Locate cells.
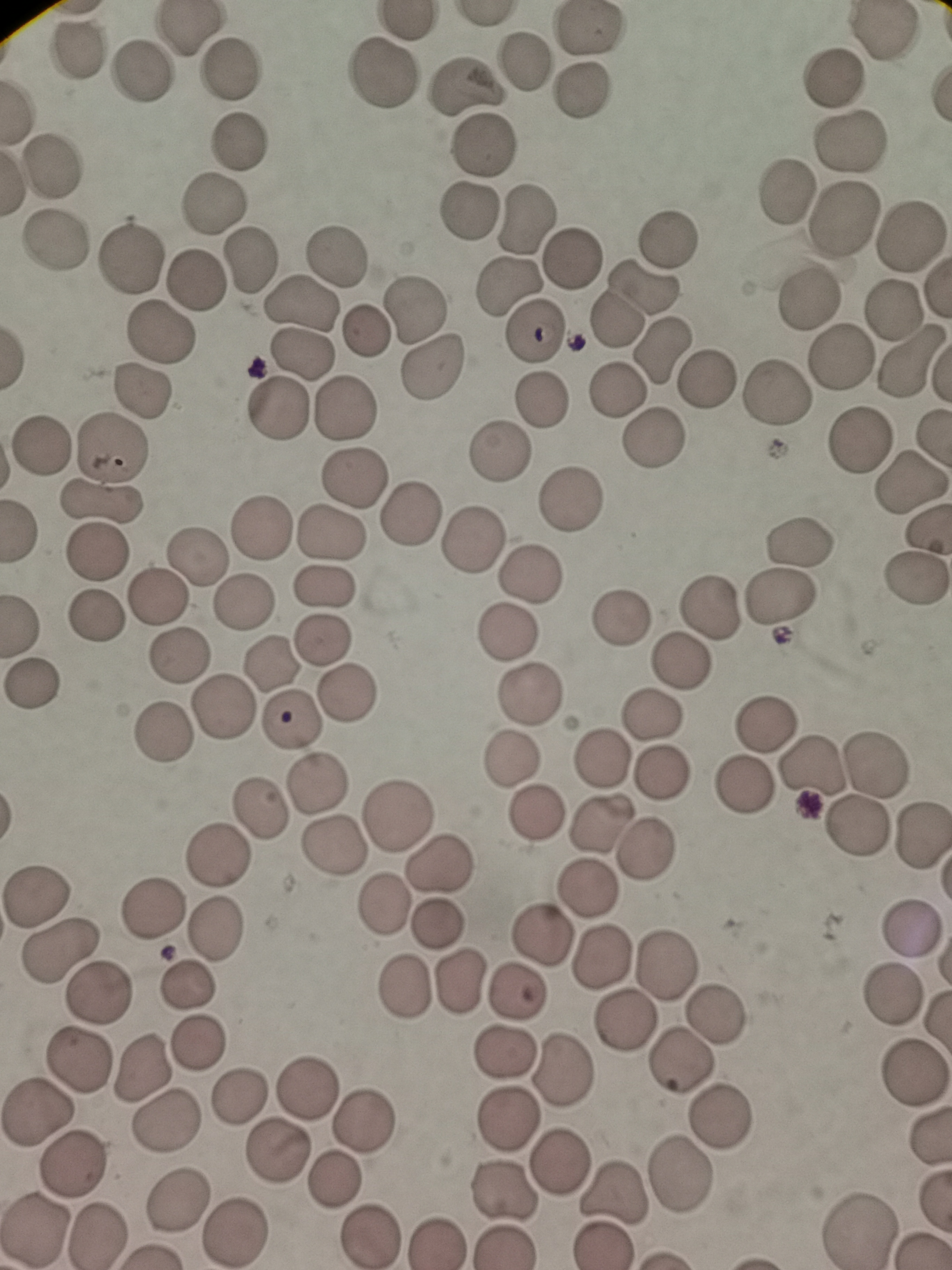
Approximate centers as {x, y} in pixels.
Cells: {588, 27}, {77, 47}, {522, 60}, {227, 69}, {142, 72}, {382, 74}, {829, 79}, {465, 85}, {581, 93}, {240, 138}, {851, 142}, {485, 145}, {53, 165}, {786, 192}, {214, 205}, {471, 208}, {843, 218}, {523, 219}, {911, 234}, {673, 236}, {55, 242}, {339, 253}, {130, 257}, {251, 259}, {572, 259}, {197, 280}, {644, 285}, {508, 286}, {302, 300}, {809, 303}, {418, 304}, {895, 311}, {614, 322}, {366, 329}, {162, 332}, {532, 332}, {662, 349}, {301, 351}, {841, 357}, {911, 360}, {434, 365}, {706, 380}, {144, 390}, {616, 391}, {776, 396}, {545, 397}, {348, 404}, {277, 409}, {653, 438}, {860, 441}, {39, 443}, {112, 448}, {497, 452}, {353, 475}, {913, 485}, {102, 502}, {569, 503}, {408, 513}, {263, 525}, {331, 535}, {801, 537}, {475, 540}, {95, 551}, {197, 559}, {530, 572}, {322, 588}, {155, 597}, {784, 597}, {243, 602}, {710, 608}, {95, 617}, {624, 622}, {509, 633}, {319, 640}, {181, 656}, {680, 661}, {269, 667}, {346, 692}, {531, 695}, {223, 708}, {652, 714}, {292, 718}, {766, 722}, {600, 758}, {874, 760}, {514, 762}, {815, 766}, {313, 778}, {741, 787}, {402, 806}, {259, 808}, {537, 813}, {855, 823}, {600, 825}, {921, 839}, {329, 846}, {644, 848}, {217, 857}, {444, 861}, {587, 892}, {36, 895}, {379, 905}, {151, 908}, {437, 925}, {218, 928}, {909, 930}, {540, 939}, {60, 947}, {601, 954}, {663, 961}, {460, 983}, {188, 987}, {400, 988}, {98, 989}, {514, 992}, {892, 994}, {716, 1011}, {619, 1023}, {201, 1044}, {503, 1053}, {79, 1063}, {685, 1063}, {141, 1066}, {564, 1068}, {911, 1071}, {307, 1087}, {237, 1098}, {40, 1112}, {714, 1117}, {165, 1121}, {507, 1122}, {362, 1124}, {276, 1153}, {72, 1158}, {562, 1163}, {681, 1172}, {335, 1179}, {507, 1191}, {614, 1194}, {177, 1203}, {861, 1226}, {235, 1228}, {32, 1231}, {370, 1233}, {98, 1235}, {438, 1240}.

field of view = single
capture = smartphone camera at the microscope eyepiece
stain = Giemsa
preparation = thin smear
image size = 952×1270 pixels